State the blood parasite species.
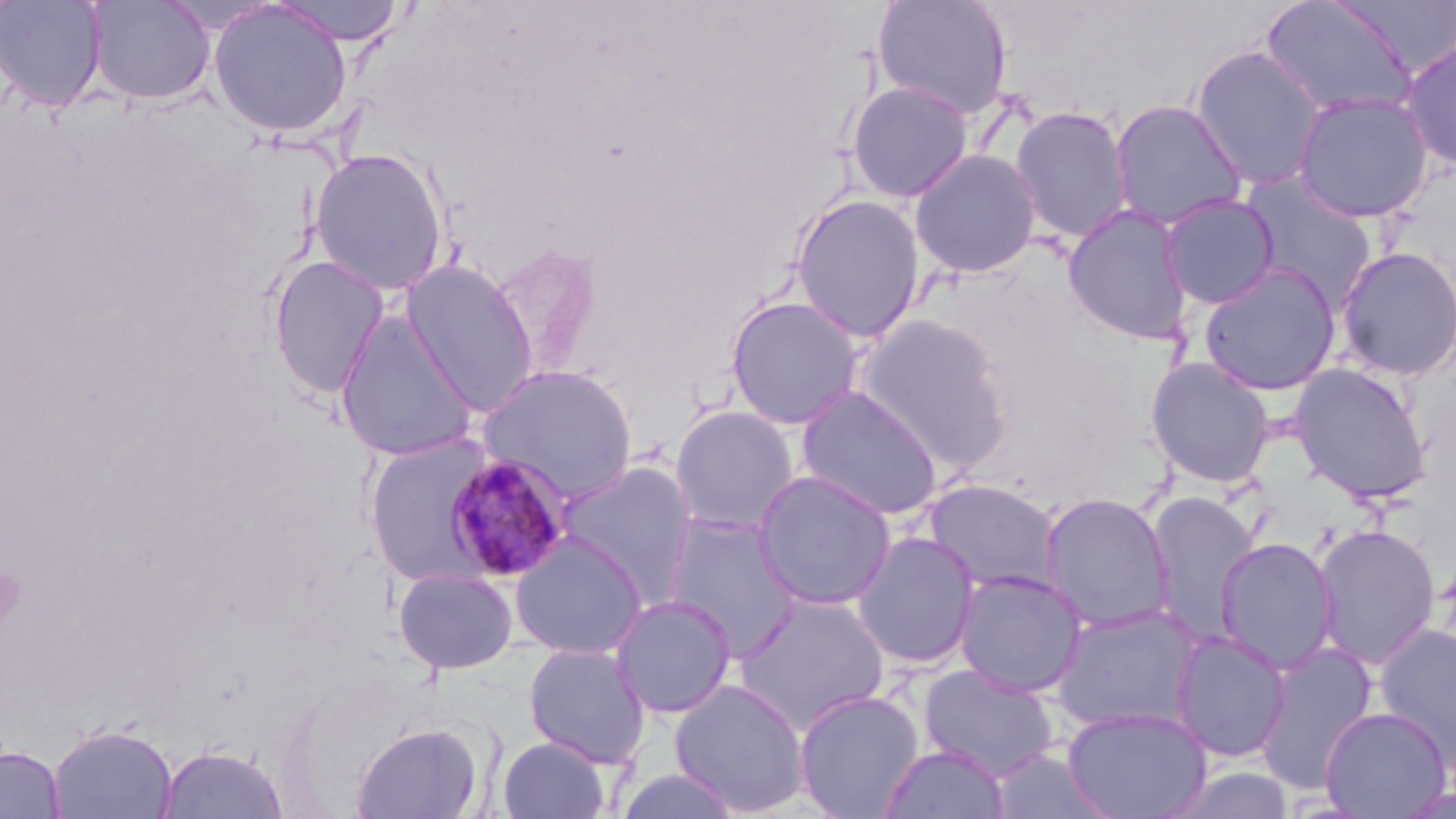
Plasmodium malariae.

Approximate bounding boxes as named x1/y1/x2/y2 corners in pixels. Uninfected red blood cell locations: (x1=0, y1=0, x2=109, y2=112), (x1=86, y1=0, x2=216, y2=105), (x1=272, y1=0, x2=408, y2=45), (x1=871, y1=0, x2=1013, y2=120), (x1=209, y1=1, x2=353, y2=138), (x1=1260, y1=1, x2=1420, y2=121), (x1=1399, y1=36, x2=1456, y2=172), (x1=1189, y1=45, x2=1326, y2=191), (x1=845, y1=80, x2=974, y2=203), (x1=1292, y1=91, x2=1434, y2=223), (x1=1109, y1=99, x2=1248, y2=231), (x1=1009, y1=105, x2=1132, y2=243), (x1=310, y1=148, x2=449, y2=295), (x1=909, y1=148, x2=1042, y2=278), (x1=1238, y1=171, x2=1378, y2=309), (x1=790, y1=193, x2=926, y2=342), (x1=1159, y1=194, x2=1280, y2=309), (x1=1061, y1=203, x2=1195, y2=345), (x1=487, y1=241, x2=605, y2=378), (x1=1334, y1=246, x2=1456, y2=381), (x1=267, y1=254, x2=391, y2=399), (x1=399, y1=259, x2=539, y2=416), (x1=1199, y1=263, x2=1341, y2=396), (x1=724, y1=295, x2=865, y2=430), (x1=334, y1=309, x2=479, y2=462), (x1=854, y1=314, x2=1016, y2=475), (x1=1145, y1=356, x2=1275, y2=488), (x1=1289, y1=362, x2=1434, y2=505), (x1=476, y1=363, x2=638, y2=503), (x1=795, y1=384, x2=945, y2=520), (x1=668, y1=404, x2=801, y2=535), (x1=364, y1=432, x2=500, y2=584), (x1=554, y1=460, x2=700, y2=603), (x1=751, y1=470, x2=897, y2=611), (x1=922, y1=479, x2=1063, y2=598), (x1=1145, y1=489, x2=1260, y2=648), (x1=1039, y1=491, x2=1176, y2=633), (x1=662, y1=512, x2=804, y2=661), (x1=1313, y1=523, x2=1441, y2=670), (x1=851, y1=530, x2=981, y2=669), (x1=509, y1=531, x2=649, y2=660), (x1=1215, y1=536, x2=1338, y2=674), (x1=393, y1=568, x2=518, y2=674), (x1=953, y1=568, x2=1088, y2=698), (x1=732, y1=592, x2=890, y2=734), (x1=609, y1=594, x2=738, y2=719), (x1=1050, y1=604, x2=1204, y2=734), (x1=1372, y1=623, x2=1455, y2=768), (x1=1169, y1=631, x2=1292, y2=762), (x1=523, y1=643, x2=651, y2=767), (x1=1253, y1=643, x2=1379, y2=795), (x1=917, y1=664, x2=1061, y2=781), (x1=669, y1=677, x2=812, y2=816), (x1=793, y1=688, x2=924, y2=818), (x1=1061, y1=706, x2=1213, y2=819), (x1=1319, y1=706, x2=1451, y2=818), (x1=351, y1=720, x2=485, y2=819), (x1=47, y1=723, x2=178, y2=819), (x1=496, y1=736, x2=611, y2=819), (x1=156, y1=743, x2=289, y2=818), (x1=878, y1=744, x2=1009, y2=819), (x1=0, y1=747, x2=65, y2=818). Plasmodium malariae-infected red blood cell locations: (x1=442, y1=452, x2=574, y2=583). One field of a larger specimen. Light microscopy. May-Grünwald-Giemsa stain. Captured at 1000x magnification. Image is 1456×819 pixels. Thin blood smear.